Comment on the morphology of the erythrocytes.
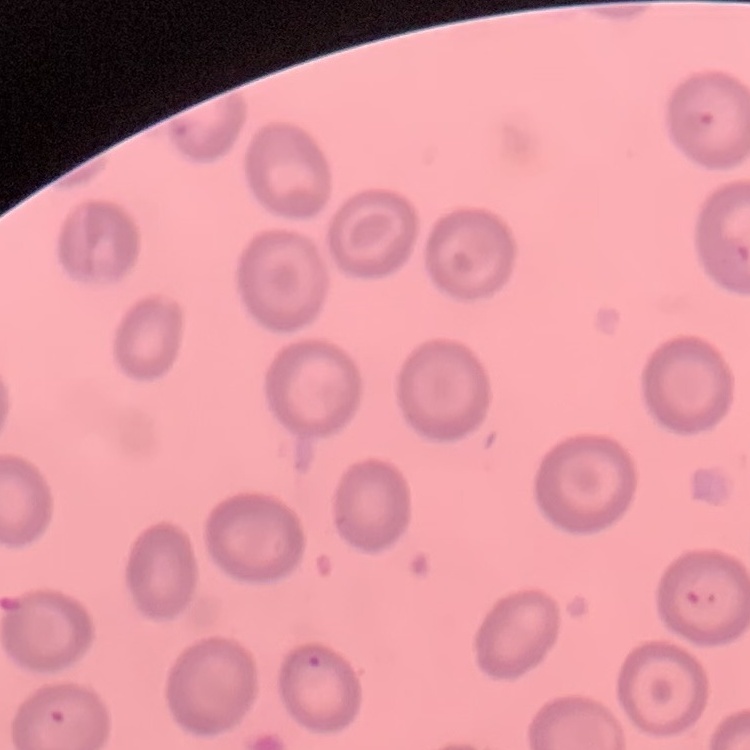
No rouleaux formation.

Summary:
  - Stain: Field's or Giemsa
  - Image type: one tile cut from a larger photomicrograph
  - Preparation: thin peripheral smear